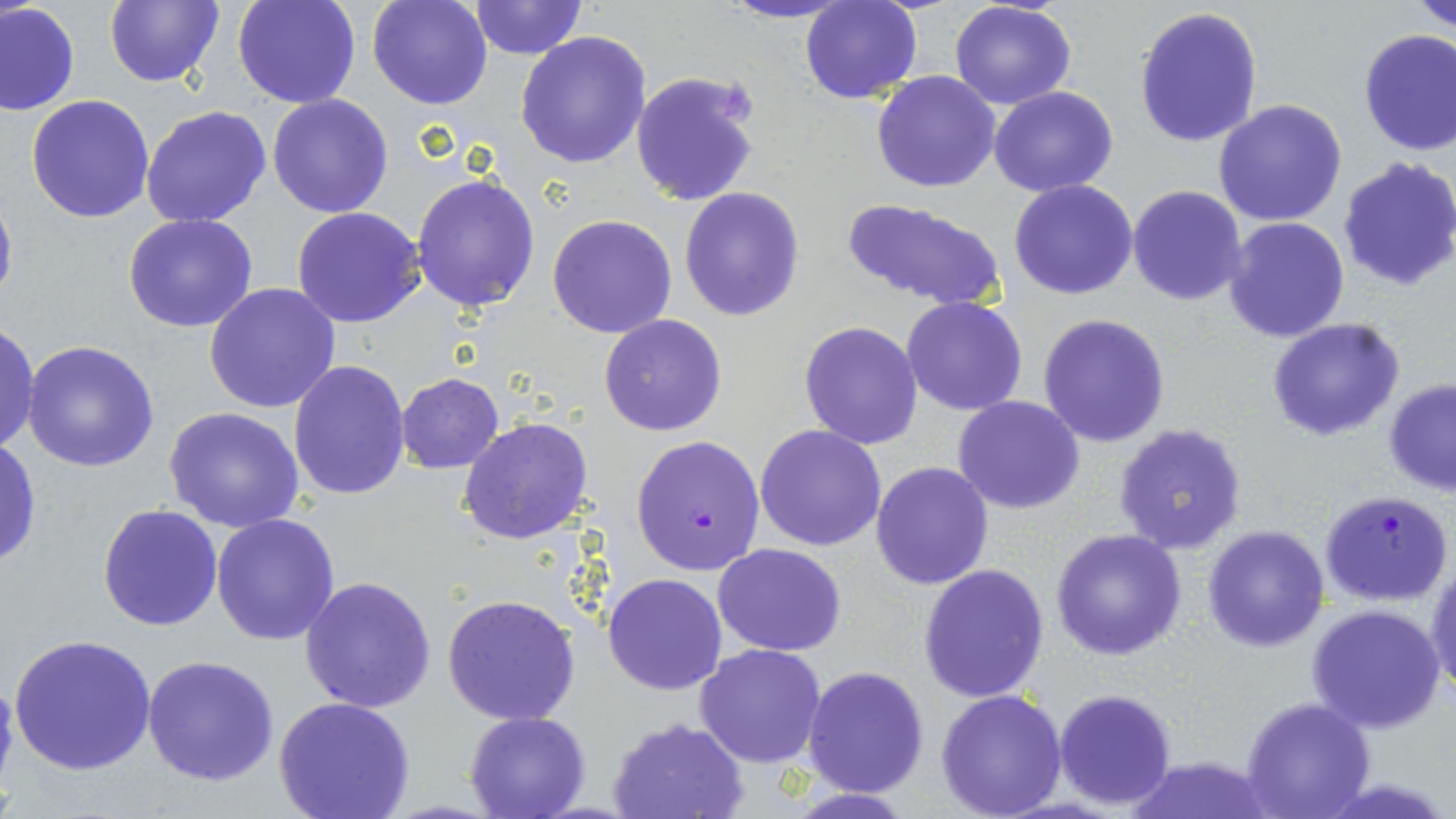 Approximate bounding boxes as [x1, y1, x2, y2] in pixels. Uninfected red blood cell locations: [102, 0, 224, 88], [232, 0, 362, 108], [367, 0, 493, 110], [467, 0, 587, 57], [716, 0, 859, 24], [800, 0, 923, 103], [1409, 0, 1456, 33], [948, 1, 1077, 110], [1, 2, 80, 115], [1132, 5, 1263, 149], [1357, 29, 1456, 159], [515, 30, 653, 169], [630, 70, 761, 208], [871, 70, 1002, 193], [989, 86, 1118, 197], [266, 93, 393, 218], [26, 94, 157, 223], [1214, 98, 1350, 227], [141, 104, 274, 228], [1336, 158, 1456, 291], [411, 173, 542, 314], [0, 179, 17, 315], [1010, 179, 1139, 300], [678, 186, 805, 323], [1127, 186, 1247, 306], [840, 198, 1009, 312], [293, 207, 427, 330], [122, 213, 259, 332], [548, 214, 678, 339], [1223, 217, 1350, 341], [205, 282, 341, 413], [901, 295, 1029, 417], [1037, 313, 1171, 448], [599, 315, 727, 437], [1266, 318, 1406, 441], [0, 320, 39, 455], [798, 320, 924, 449], [0, 327, 82, 460], [21, 341, 160, 472], [289, 361, 411, 501], [395, 374, 505, 474], [1382, 378, 1456, 496], [953, 397, 1085, 514], [165, 408, 305, 534], [458, 417, 590, 545], [1114, 423, 1247, 555], [755, 424, 887, 551], [0, 437, 41, 570], [871, 461, 995, 590], [96, 503, 222, 632], [211, 513, 342, 647], [1201, 524, 1330, 652], [1049, 529, 1188, 661], [714, 542, 845, 656], [1426, 561, 1456, 696], [918, 564, 1050, 704], [604, 572, 727, 695], [299, 575, 438, 713], [441, 594, 584, 726], [1304, 603, 1448, 735], [9, 634, 158, 776], [694, 642, 826, 768], [142, 656, 280, 786], [802, 666, 929, 796], [0, 671, 19, 795], [1053, 688, 1177, 810], [935, 689, 1069, 818], [273, 696, 417, 819], [1239, 697, 1375, 819], [464, 711, 590, 819], [608, 716, 749, 819], [1127, 757, 1272, 819]. Plasmodium falciparum-infected red blood cell locations: [631, 434, 766, 576], [1320, 489, 1453, 606]. Slide-level diagnosis: Plasmodium falciparum. Image is 1456×819 pixels. Light microscopy. Thin blood smear. Single field of view. May-Grünwald-Giemsa stain. Captured at 1000x magnification.